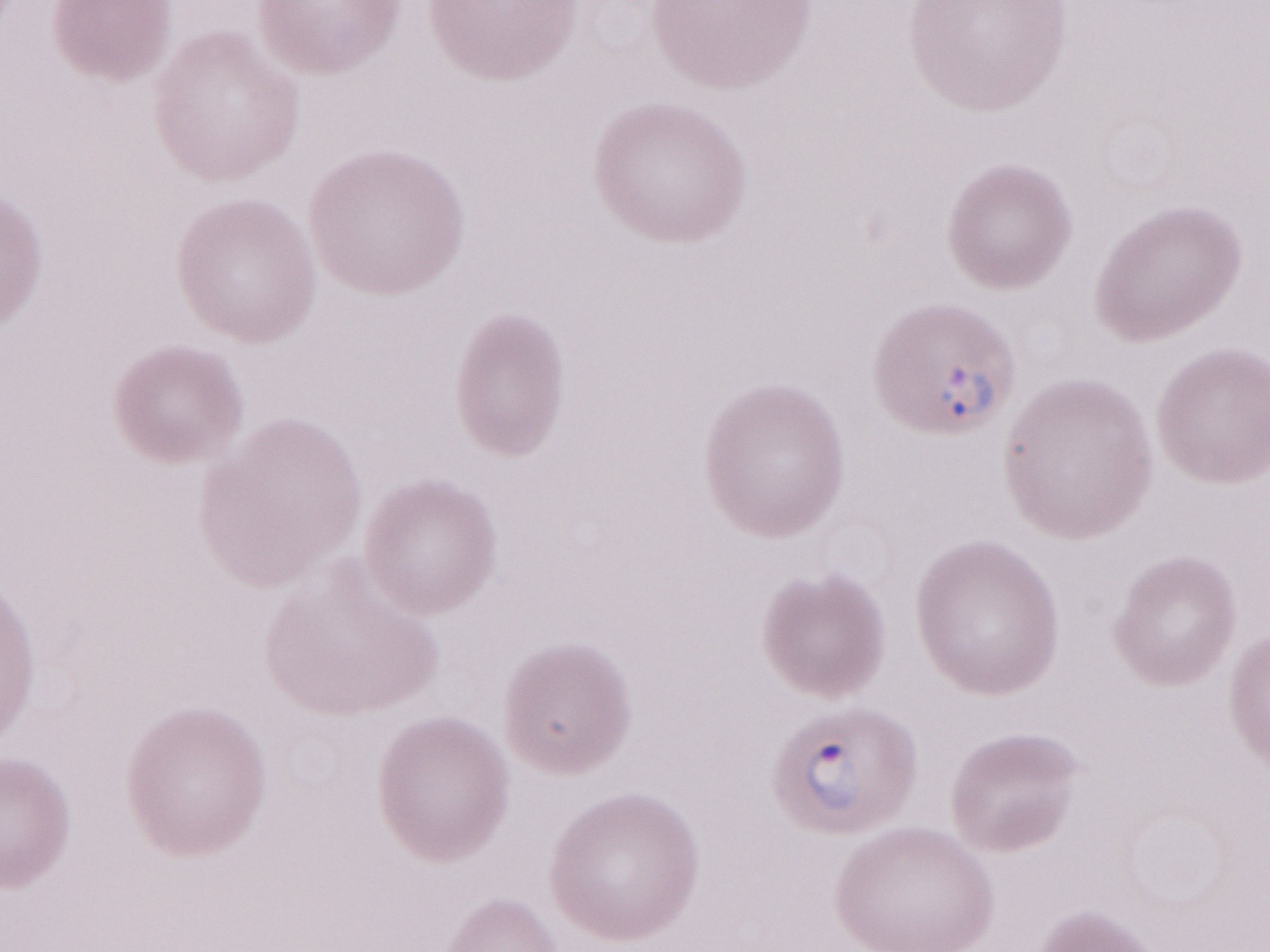
Image is 1270×952 pixels. Single field of view. May-Grünwald-Giemsa-stained preparation. Patient-level malaria diagnosis: positive. Olympus BX43 microscope, Olympus DP73 camera. Thin blood film. 1,000x magnification.